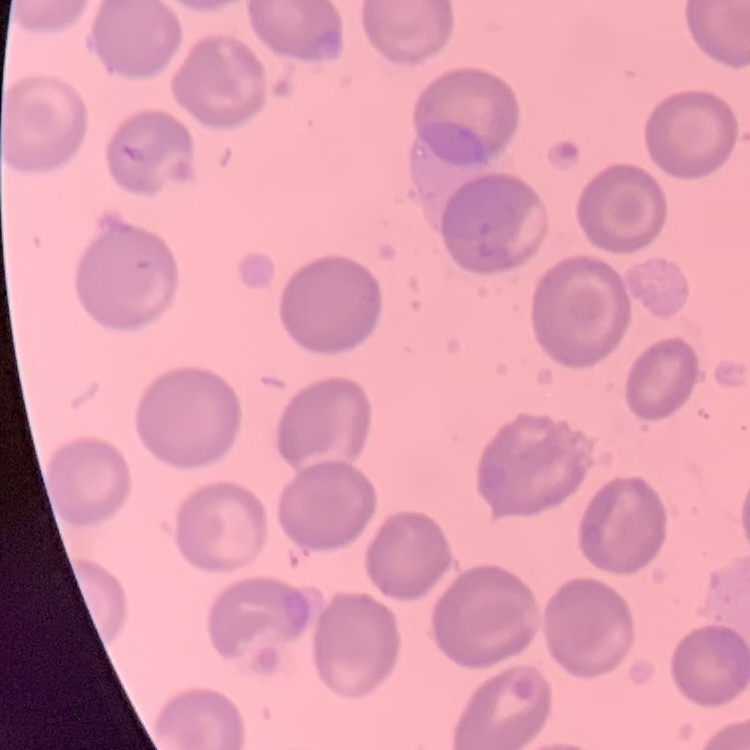
The erythrocytes show no rouleaux formation. Thin peripheral smear. Stained with either Field's or Giemsa. One tile cut from a larger photomicrograph.